Identify the parasite.
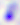

Toxoplasma gondii.

Micrograph. Captured at 400x magnification.